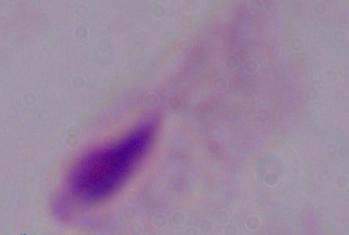

{
  "modality": "photomicrograph",
  "identification": "trichomonad",
  "magnification": "1000x"
}